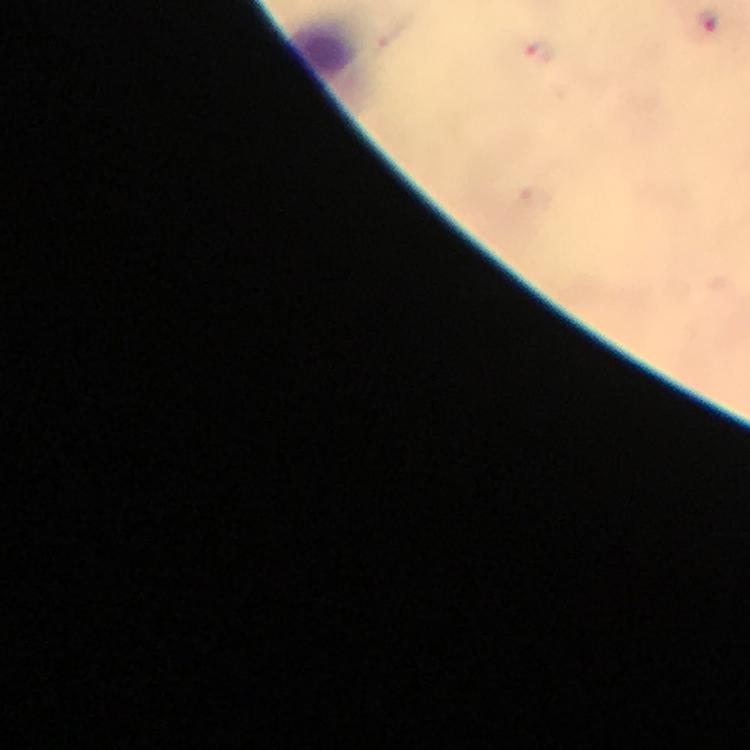

Approximate centers as [x, y] in pixels.
Summary:
  - Plasmodium parasite locations: [706, 22], [539, 53]
  - Cropped from: a single field of view
  - Image size: 750×750 pixels
  - Context: from a diagnostic examination for malaria
  - Magnification: 100x
  - Preparation: thick blood film
  - Capture: smartphone photograph through a microscope
  - Immersion oil: applied
  - Stain: Giemsa